Assess this cell for malaria.
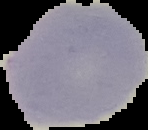
It is uninfected.

The area outside the segmented cell region is set to black. From a thin blood film. Image is 148×130 pixels.